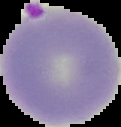

Image is 121×127 pixels. Result: Plasmodium parasites detected. The area outside the segmented cell region is set to black. From a thin blood smear.